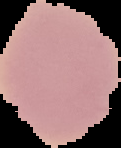
Summary:
  - Image size: 121×148 pixels
  - Preparation: thin blood smear
  - Image type: segmented cell region with the area outside set to black
  - Result: negative for Plasmodium parasites